Comment on the morphology of the erythrocytes.
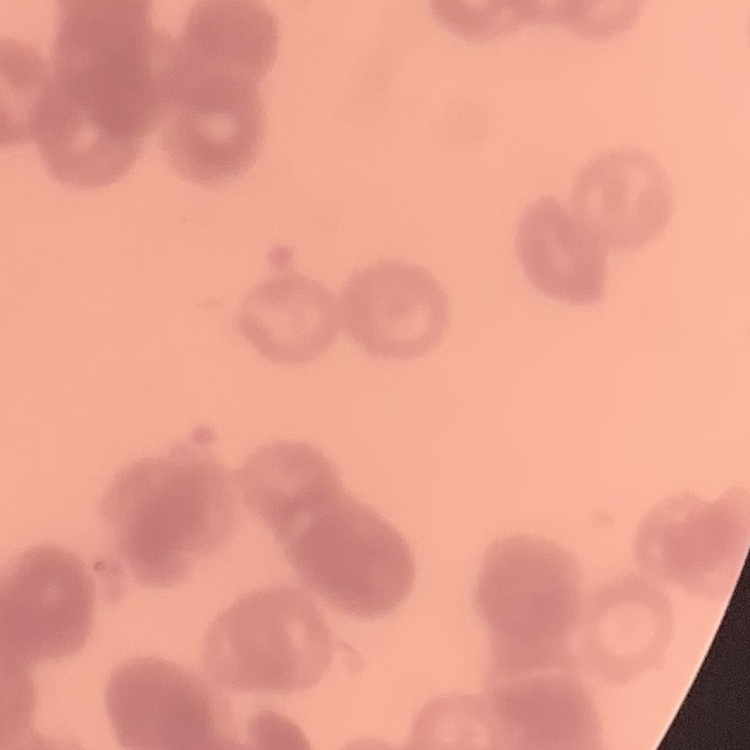
Rouleaux formation.

Stained with either Field's or Giemsa. Square crop of a larger photomicrograph. Thin blood smear.